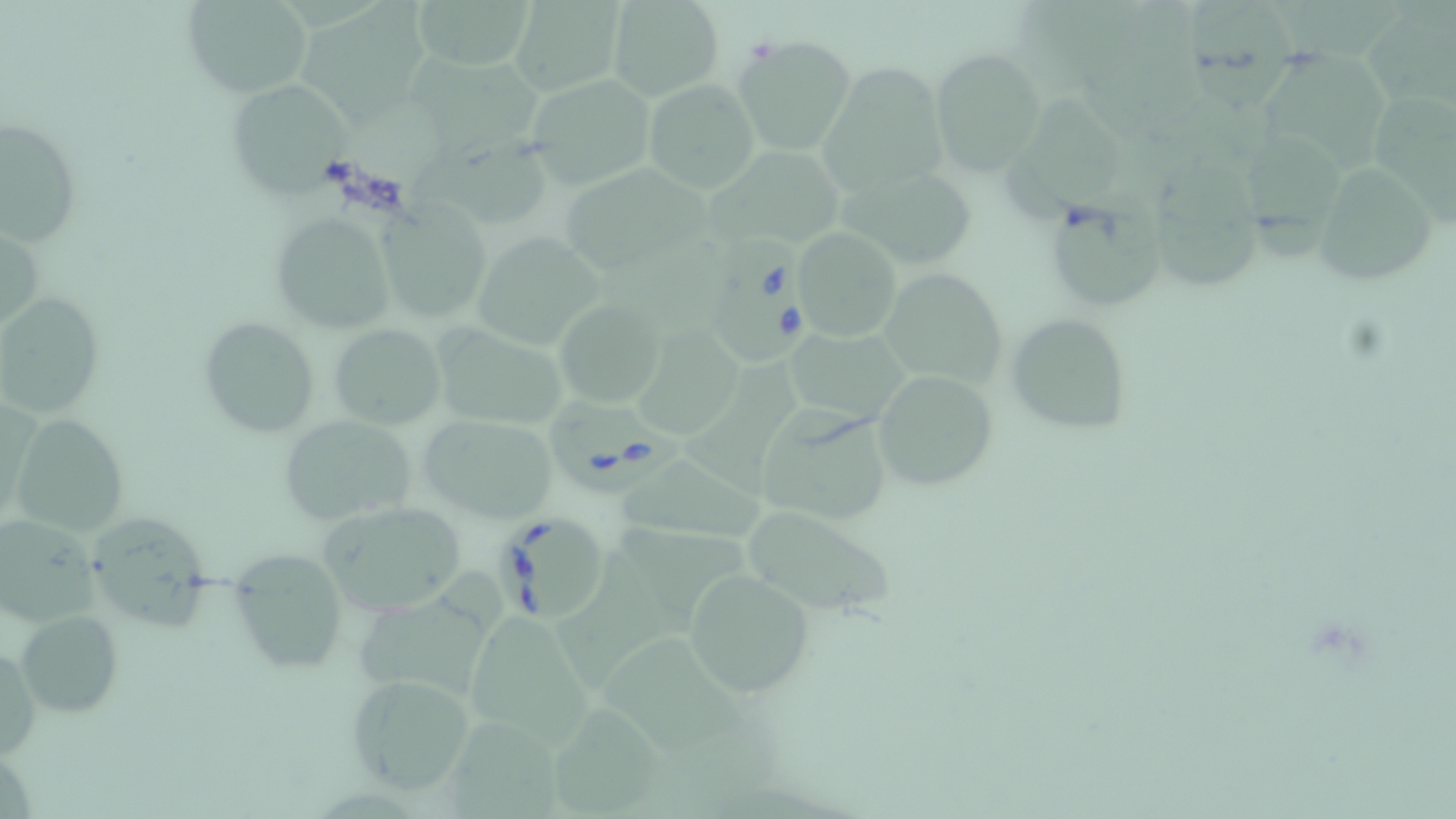 Approximate bounding boxes as named x1/y1/x2/y2 corners in pixels. Babesia divergens-infected red blood cell locations: (x1=705, y1=230, x2=817, y2=367), (x1=548, y1=399, x2=686, y2=494), (x1=494, y1=514, x2=612, y2=625). Uninfected red blood cell locations: (x1=408, y1=0, x2=540, y2=73), (x1=1183, y1=0, x2=1301, y2=116), (x1=1274, y1=0, x2=1412, y2=65), (x1=180, y1=1, x2=311, y2=98), (x1=506, y1=1, x2=628, y2=96), (x1=296, y1=3, x2=444, y2=130), (x1=605, y1=3, x2=723, y2=102), (x1=1360, y1=3, x2=1456, y2=111), (x1=732, y1=35, x2=855, y2=156), (x1=1255, y1=48, x2=1390, y2=182), (x1=929, y1=49, x2=1047, y2=176), (x1=407, y1=53, x2=553, y2=156), (x1=817, y1=65, x2=951, y2=194), (x1=525, y1=73, x2=658, y2=189), (x1=229, y1=79, x2=356, y2=200), (x1=644, y1=79, x2=760, y2=193), (x1=1004, y1=90, x2=1133, y2=222), (x1=1373, y1=94, x2=1456, y2=226), (x1=1, y1=118, x2=82, y2=245), (x1=1236, y1=122, x2=1350, y2=261), (x1=407, y1=139, x2=556, y2=232), (x1=705, y1=145, x2=848, y2=252), (x1=1313, y1=161, x2=1441, y2=288), (x1=562, y1=164, x2=718, y2=275), (x1=834, y1=164, x2=981, y2=270), (x1=1151, y1=174, x2=1257, y2=293), (x1=1052, y1=187, x2=1166, y2=315), (x1=376, y1=200, x2=492, y2=324), (x1=270, y1=213, x2=396, y2=336), (x1=0, y1=220, x2=45, y2=341), (x1=792, y1=228, x2=903, y2=342), (x1=470, y1=233, x2=604, y2=350), (x1=878, y1=268, x2=1008, y2=390), (x1=1, y1=290, x2=107, y2=416), (x1=554, y1=298, x2=665, y2=408), (x1=632, y1=301, x2=744, y2=438), (x1=1006, y1=312, x2=1133, y2=435), (x1=199, y1=317, x2=322, y2=439), (x1=331, y1=323, x2=446, y2=430), (x1=431, y1=327, x2=566, y2=430), (x1=785, y1=329, x2=915, y2=422), (x1=693, y1=353, x2=805, y2=492), (x1=872, y1=369, x2=1000, y2=493), (x1=757, y1=407, x2=893, y2=526), (x1=415, y1=414, x2=559, y2=524), (x1=11, y1=415, x2=129, y2=537), (x1=281, y1=416, x2=417, y2=525), (x1=621, y1=459, x2=777, y2=547), (x1=318, y1=500, x2=464, y2=613), (x1=739, y1=504, x2=896, y2=619), (x1=1, y1=514, x2=110, y2=623), (x1=93, y1=520, x2=215, y2=643), (x1=616, y1=527, x2=755, y2=637), (x1=557, y1=543, x2=672, y2=692), (x1=236, y1=552, x2=347, y2=671), (x1=357, y1=565, x2=501, y2=694), (x1=684, y1=566, x2=814, y2=699), (x1=464, y1=609, x2=604, y2=752), (x1=16, y1=611, x2=123, y2=718), (x1=609, y1=639, x2=762, y2=770), (x1=1, y1=640, x2=42, y2=764), (x1=343, y1=671, x2=479, y2=799), (x1=543, y1=703, x2=670, y2=815), (x1=446, y1=717, x2=564, y2=819). Slide-level diagnosis: Babesia divergens. Optical microscopy. May-Grünwald-Giemsa stain. Image is 1456×819 pixels. Captured at 1000x magnification. Thin blood smear. Single field of view.